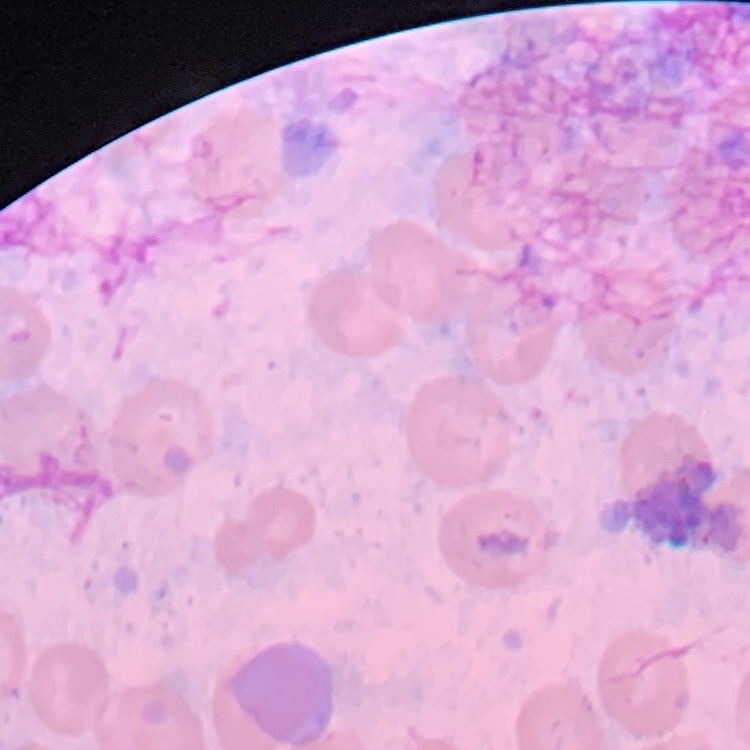
erythrocyte_morphology: no rouleaux formation
stain: Field's or Giemsa
image_type: square crop of a larger photomicrograph
preparation: thin peripheral smear